Classify this cell by malaria status.
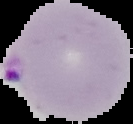

It is parasitized.

Summary:
  - Preparation: thin blood film
  - Image type: cell region segmented out of the field of view; surrounding area masked to black
  - Image size: 133×124 pixels